Classify this cell by malaria status.
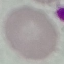
Uninfected.

Giemsa-stained preparation. Automatically extracted cell patch, resized to 64 × 64 pixels. Photographed with a smartphone camera at the microscope eyepiece. Thin smear of blood.